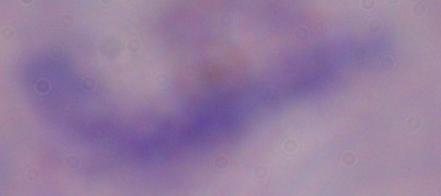

Micrograph. A trypanosome is shown. Captured at 1000x magnification.